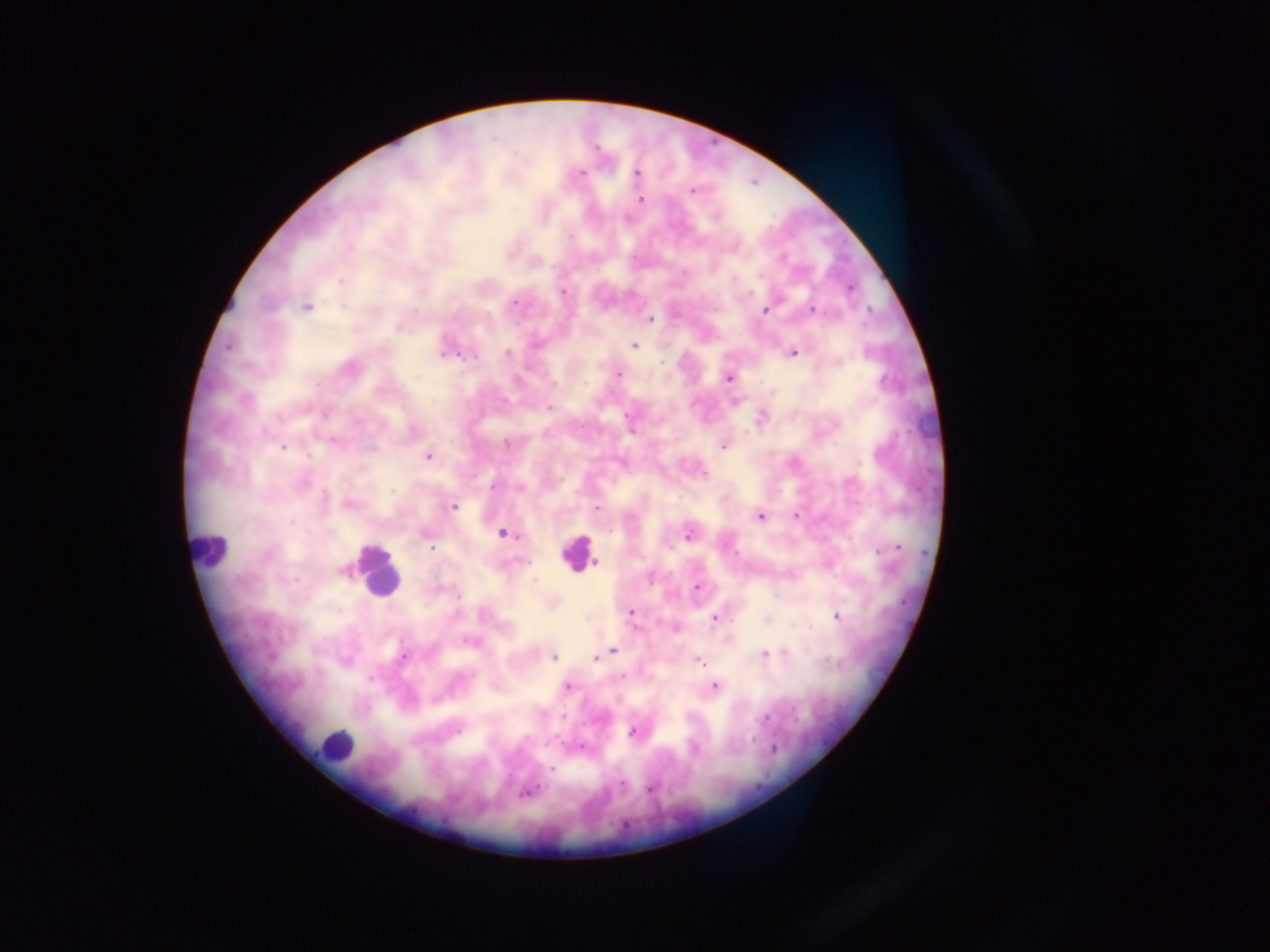 Approximate centers as {x, y} in pixels. Malaria parasite locations: {637, 173}, {581, 174}, {692, 191}, {640, 200}, {717, 216}, {569, 237}, {782, 257}, {732, 279}, {852, 287}, {562, 292}, {514, 302}, {306, 307}, {811, 309}, {765, 310}, {868, 311}, {650, 319}, {398, 328}, {536, 344}, {228, 346}, {634, 346}, {793, 352}, {508, 353}, {869, 353}, {441, 355}, {459, 356}, {662, 361}, {838, 362}, {618, 373}, {728, 378}, {554, 384}, {884, 384}, {549, 407}, {627, 415}, {414, 431}, {506, 444}, {724, 445}, {284, 447}, {428, 456}, {704, 474}, {493, 487}, {325, 496}, {350, 505}, {453, 506}, {598, 509}, {760, 516}, {796, 516}, {502, 533}, {424, 534}, {688, 536}, {431, 548}, {879, 549}, {892, 550}, {527, 562}, {596, 562}, {343, 570}, {696, 587}, {458, 597}, {630, 612}, {837, 617}, {714, 618}, {767, 620}, {613, 650}, {764, 654}, {403, 657}, {553, 657}, {596, 659}, {700, 662}, {621, 677}, {370, 679}, {568, 687}, {715, 687}, {793, 709}, {562, 716}, {766, 718}, {459, 730}, {633, 731}, {752, 739}, {582, 747}, {774, 749}, {552, 769}, {620, 783}, {649, 789}, {527, 793}. Leukocyte locations: {209, 548}, {577, 554}, {377, 573}, {336, 744}. Photographed through a microscope with a mobile-phone camera. Collected in Ghana. One field of view. Image is 1270×952 pixels. Thick blood smear.